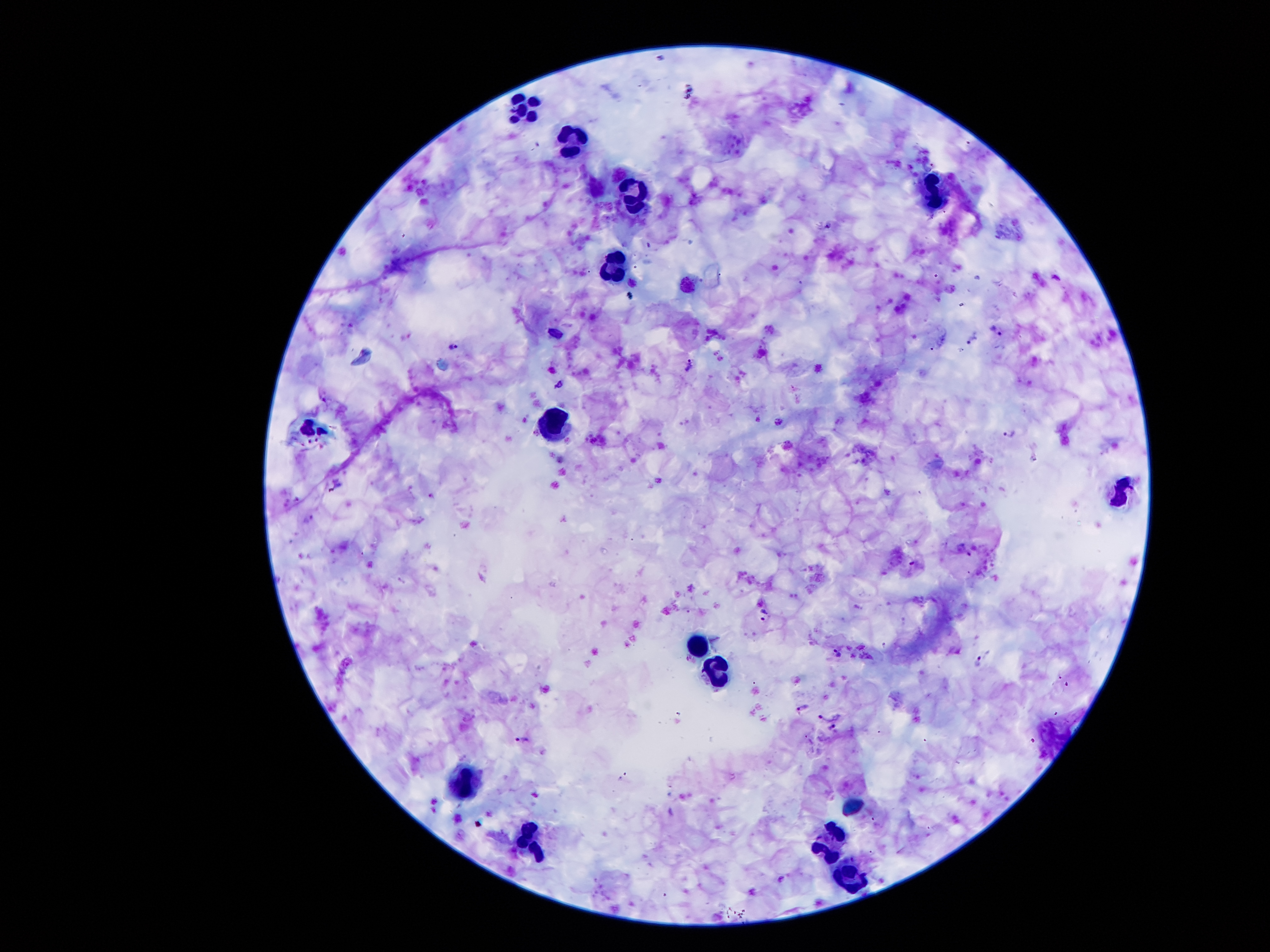

coordinate format = approximate object centers, in pixels from the top-left corner
malaria parasite locations = (x=827, y=225), (x=631, y=294), (x=997, y=329), (x=973, y=340), (x=454, y=346), (x=690, y=366), (x=560, y=382), (x=779, y=422), (x=1009, y=433), (x=766, y=615), (x=837, y=651), (x=980, y=662), (x=803, y=706), (x=834, y=731), (x=522, y=738)
leukocyte locations = (x=515, y=104), (x=576, y=143), (x=932, y=191), (x=633, y=193), (x=610, y=266), (x=554, y=421), (x=1122, y=493), (x=697, y=647), (x=714, y=672), (x=468, y=782), (x=829, y=837), (x=531, y=838), (x=846, y=877)
patient malaria status = positive for Plasmodium falciparum
stain = Giemsa
capture = smartphone camera through the microscope eyepiece
field of view = one from this slide
preparation = thick blood film
image size = 1270×952 pixels
magnification = 100x